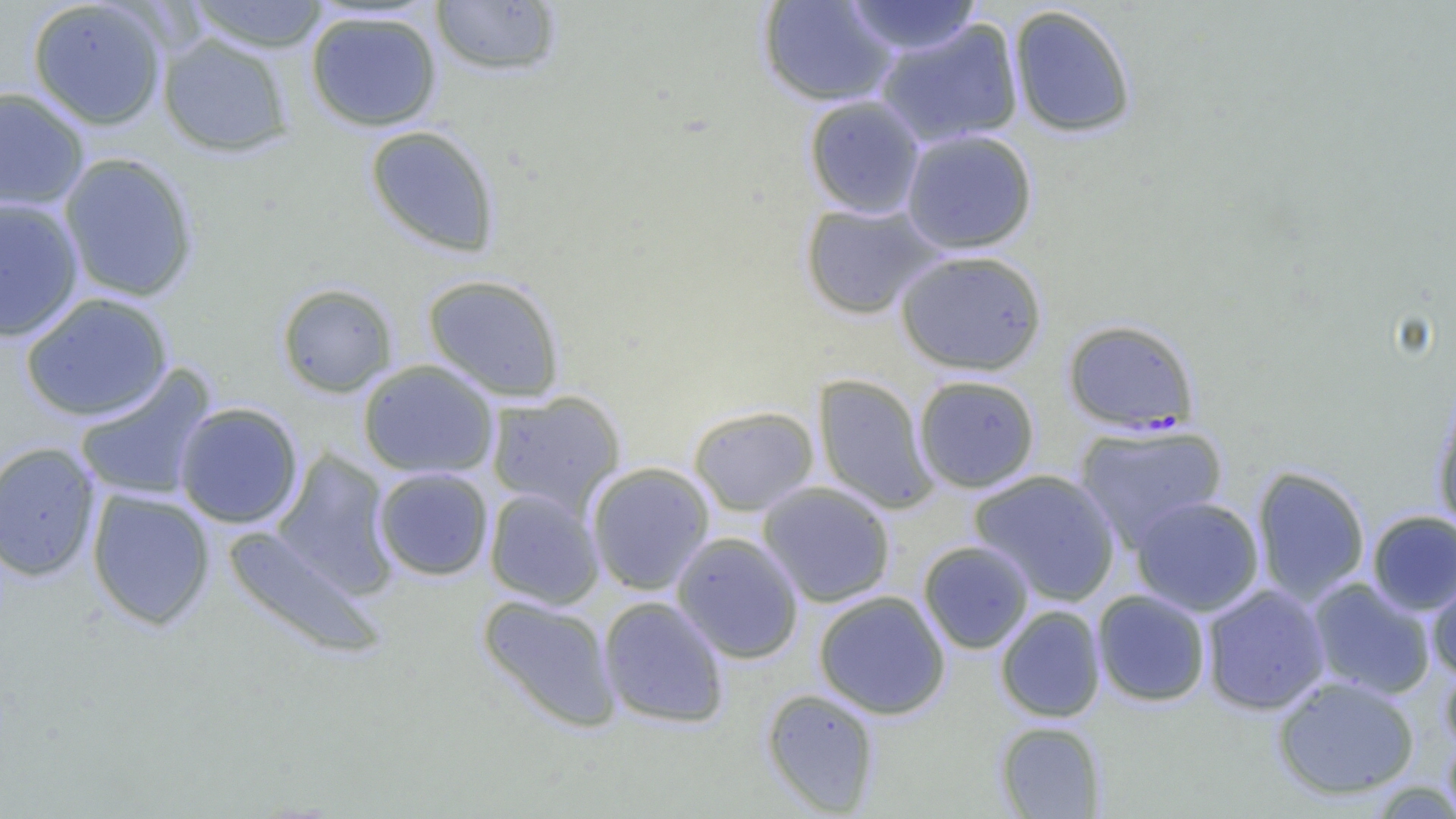

Approximate bounding boxes as [x1, y1, x2, y2] in pixels. Plasmodium falciparum-infected red blood cell locations: [1062, 318, 1201, 434]. Uninfected red blood cell locations: [27, 0, 168, 131], [185, 0, 331, 53], [429, 0, 564, 78], [757, 0, 900, 108], [841, 1, 983, 59], [1007, 4, 1138, 139], [304, 9, 443, 132], [874, 17, 1025, 148], [157, 32, 295, 157], [0, 86, 90, 211], [803, 95, 926, 218], [364, 125, 501, 258], [900, 128, 1039, 254], [58, 152, 200, 303], [0, 196, 84, 342], [799, 200, 944, 320], [894, 249, 1048, 377], [422, 273, 566, 401], [276, 282, 399, 398], [20, 292, 173, 423], [357, 360, 499, 479], [73, 365, 218, 503], [812, 373, 939, 514], [913, 374, 1041, 493], [485, 390, 626, 516], [1432, 398, 1456, 537], [173, 402, 304, 529], [687, 405, 820, 517], [1074, 422, 1228, 552], [0, 441, 101, 582], [271, 449, 397, 599], [585, 462, 716, 596], [1251, 466, 1371, 605], [372, 467, 494, 581], [969, 469, 1121, 606], [757, 481, 896, 608], [86, 488, 216, 630], [484, 488, 605, 610], [1130, 496, 1265, 616], [1367, 510, 1456, 615], [222, 525, 387, 660], [671, 532, 805, 664], [917, 540, 1035, 654], [1425, 567, 1456, 679], [1306, 577, 1438, 701], [1201, 583, 1331, 716], [813, 590, 952, 720], [1091, 590, 1211, 707], [477, 594, 622, 733], [597, 595, 730, 729], [995, 605, 1106, 722], [1440, 661, 1456, 757], [1271, 675, 1420, 800], [760, 688, 882, 816], [995, 720, 1106, 818], [1442, 730, 1456, 818]. Slide-level diagnosis: Plasmodium falciparum. 1000x magnification. One field of a larger specimen. Light microscopy. Thin blood smear. Image is 1456×819 pixels.